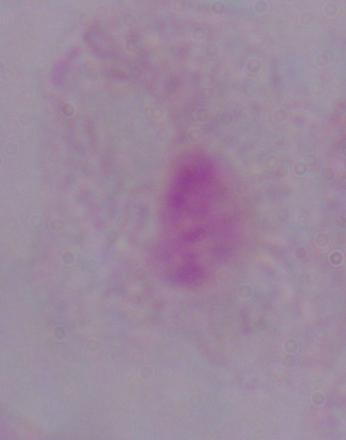
{
  "modality": "micrograph",
  "identification": "trichomonad",
  "magnification": "1000x"
}